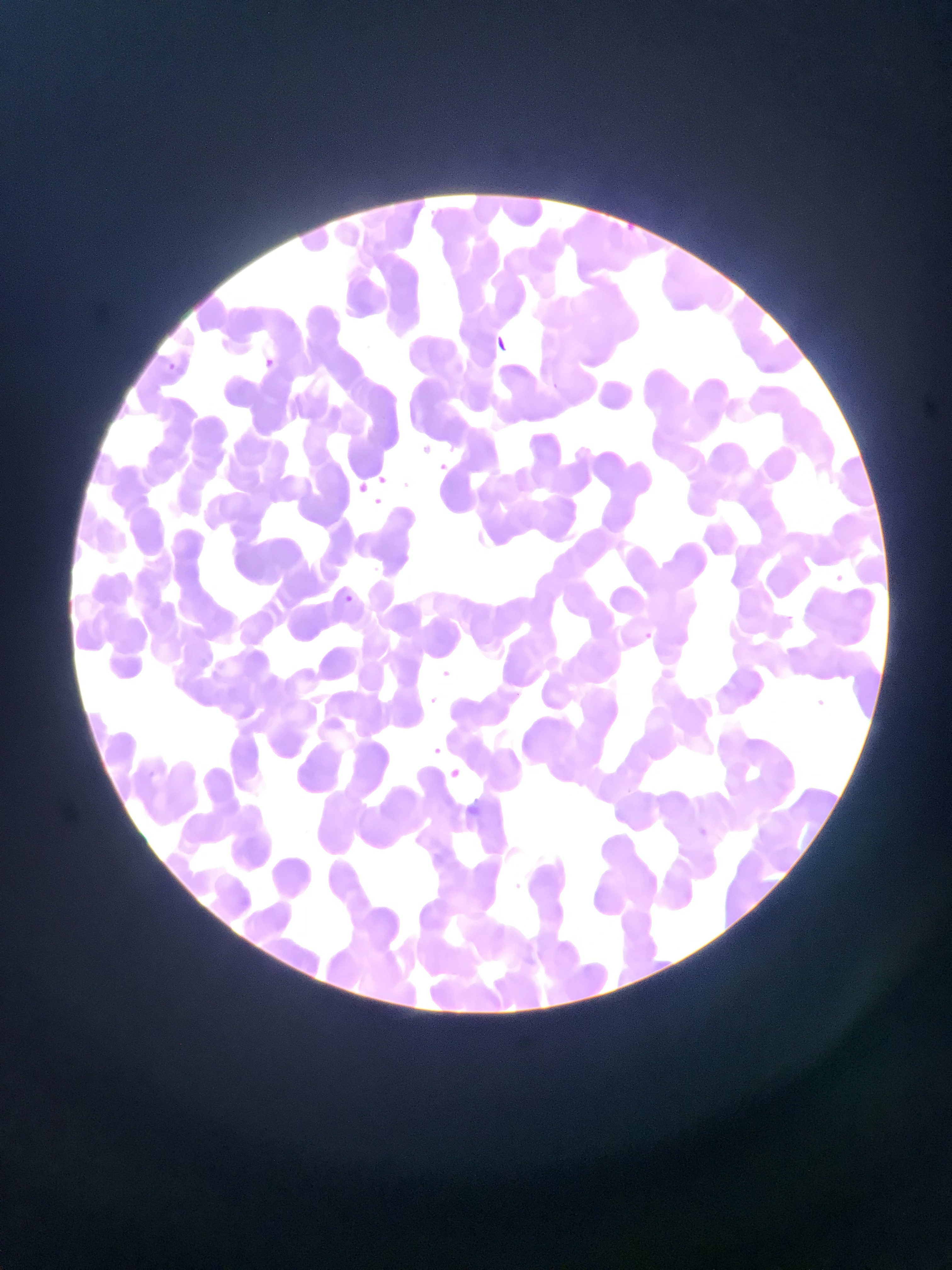
Approximate bounding boxes as [left, top, right, bottom] in pixels.
Summary:
  - Malaria parasite locations: [487, 335, 517, 362], [263, 355, 277, 372], [160, 361, 183, 374], [414, 432, 434, 445], [439, 459, 466, 478], [356, 479, 385, 498], [828, 568, 856, 584], [341, 588, 374, 620], [639, 624, 657, 647], [438, 665, 468, 685], [815, 688, 834, 708], [415, 693, 439, 705], [424, 737, 448, 756], [445, 760, 465, 783], [691, 821, 704, 832]
  - Preparation: thin blood smear
  - Capture: mobile-phone photograph through a microscope
  - Image size: 952×1270 pixels
  - Field of view: single
  - Country: Ghana